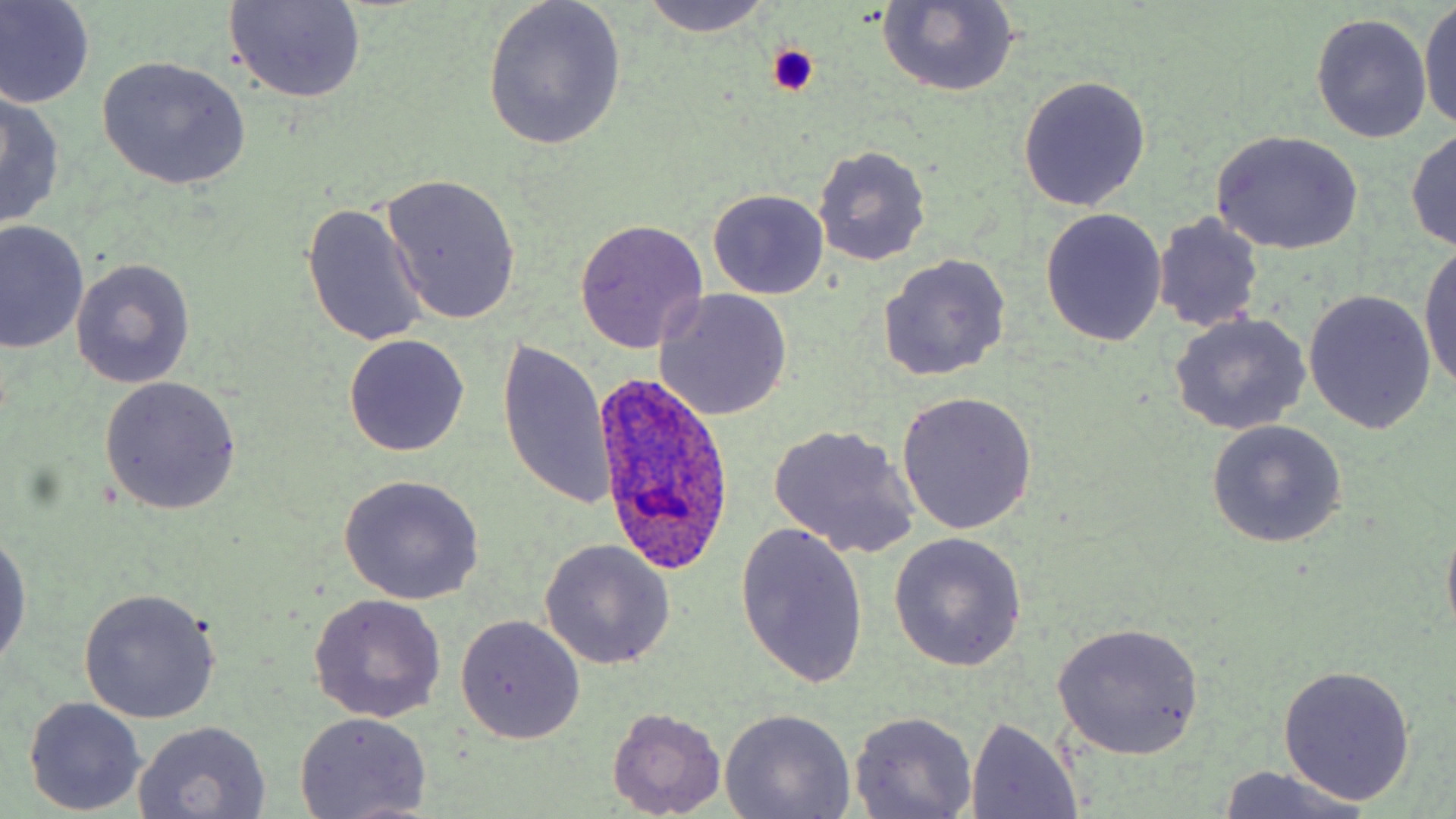

{
  "slide_level_diagnosis": "Plasmodium ovale",
  "preparation": "thin blood smear",
  "plasmodium_ovale_infected_red_blood_cell_locations": "approximate bounding boxes as (x1, y1, x2, y2) in pixels: (591, 372, 739, 577)",
  "uninfected_red_blood_cell_locations": "approximate bounding boxes as (x1, y1, x2, y2) in pixels: (480, 0, 627, 151), (637, 0, 774, 37), (878, 0, 1022, 97), (222, 1, 367, 105), (0, 2, 96, 109), (1418, 2, 1456, 133), (1310, 13, 1432, 144), (96, 56, 252, 189), (1017, 76, 1151, 212), (0, 90, 65, 229), (1407, 126, 1456, 254), (1211, 130, 1363, 255), (813, 145, 930, 265), (382, 174, 522, 326), (707, 189, 829, 300), (301, 202, 429, 348), (1039, 208, 1166, 346), (1153, 213, 1264, 332), (573, 219, 708, 352), (1, 220, 89, 357), (1418, 244, 1456, 395), (878, 254, 1010, 382), (71, 259, 195, 388), (1303, 290, 1437, 434), (655, 291, 793, 421), (1168, 313, 1311, 434), (344, 335, 469, 457), (496, 338, 613, 511), (99, 376, 242, 515), (896, 392, 1038, 535), (1206, 420, 1348, 547), (767, 423, 921, 560), (336, 476, 485, 606), (1440, 512, 1456, 646), (734, 521, 870, 692), (0, 529, 31, 675), (889, 532, 1027, 671), (540, 540, 676, 670), (77, 586, 223, 723), (307, 593, 447, 722), (455, 616, 587, 744), (1051, 623, 1206, 759), (1276, 666, 1418, 805), (23, 696, 148, 815), (606, 706, 726, 817), (720, 708, 857, 819), (848, 710, 978, 818), (295, 712, 435, 819), (965, 717, 1085, 817), (133, 721, 272, 818), (1215, 765, 1376, 819)",
  "stain": "May-Grünwald-Giemsa",
  "platelet_locations": "approximate bounding boxes as (x1, y1, x2, y2) in pixels: (764, 44, 821, 98)",
  "image_size": "1456×819 pixels",
  "magnification": "1000x",
  "modality": "optical microscopy",
  "field_of_view": "one of a larger specimen"
}